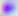

modality: photomicrograph
magnification: 400x
identification: Toxoplasma gondii